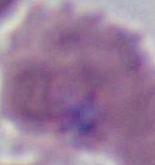
An erythrocyte is shown. Captured at 1000x magnification. Micrograph.